Point out each malaria parasite and each leukocyte.
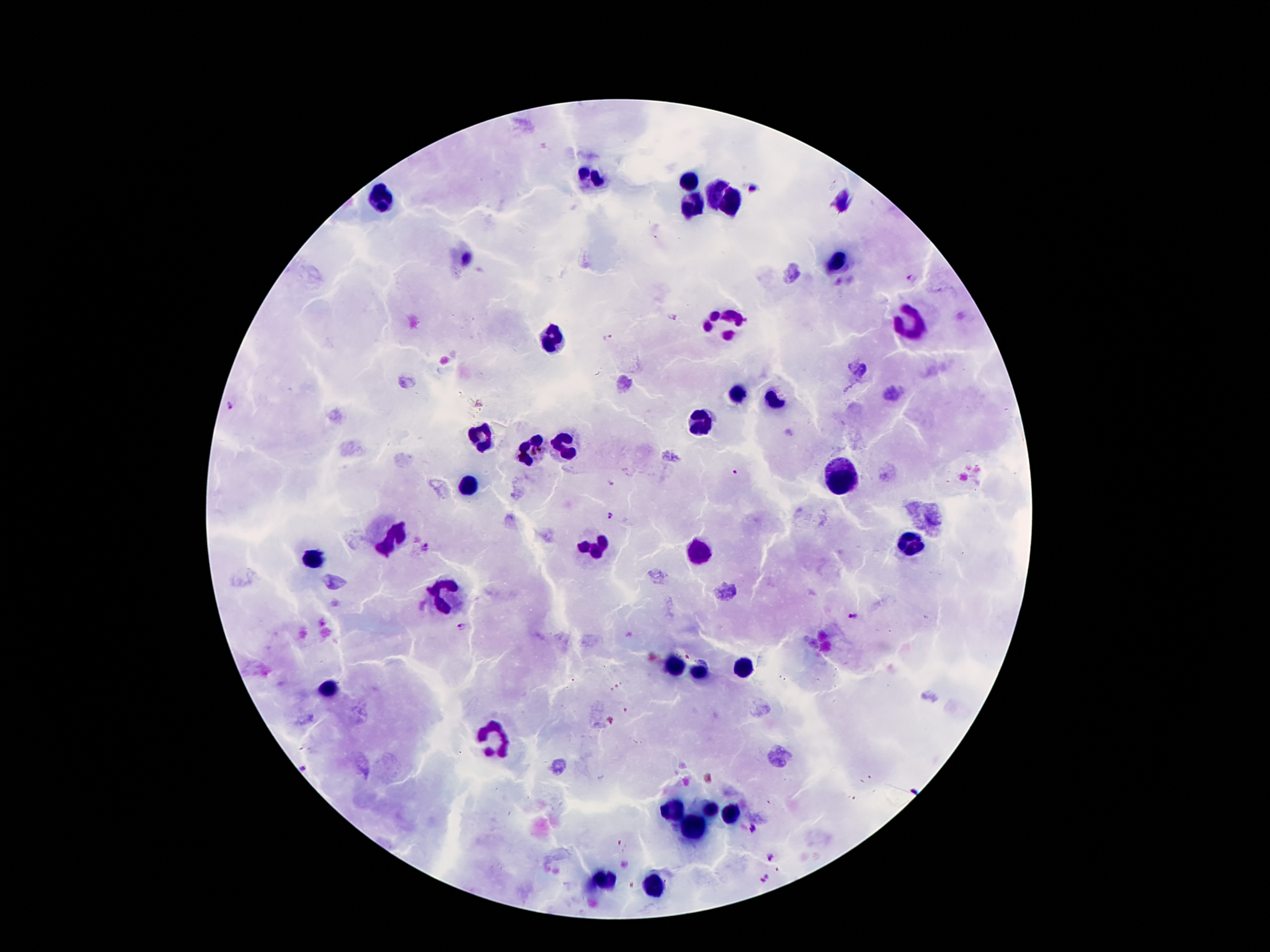

Approximate centers as (x, y) in pixels.
Malaria parasites: (754, 189), (911, 278), (671, 316), (607, 337), (610, 482), (610, 514), (424, 547), (855, 616), (461, 626), (753, 827), (772, 856), (766, 879).
Leukocytes: (594, 178), (687, 180), (712, 193), (381, 198), (697, 202), (730, 202), (835, 260), (727, 322), (908, 325), (553, 337), (738, 393), (777, 400), (700, 423), (482, 437), (562, 445), (530, 451), (839, 473), (467, 484), (392, 536), (911, 542), (596, 546), (702, 553), (316, 555), (439, 596), (672, 665), (745, 667), (702, 673), (331, 686), (489, 740), (672, 809), (708, 809), (728, 815), (691, 829), (607, 880), (654, 887).

100x magnification. Giemsa-stained preparation. Image is 1270×952 pixels. Thick blood smear. Patient malaria status: infected with Plasmodium falciparum. Smartphone photograph taken through the microscope eyepiece. One field from this slide.